State which cell type is depicted.
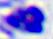
This is a leukocyte.

400x magnification. Photomicrograph.